Identify the cell.
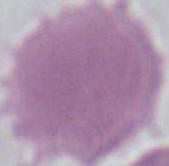

An erythrocyte.

Micrograph. Captured at 1000x magnification.